Report the malaria status of this cell.
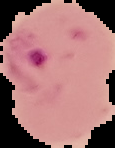
It is parasitized.

The area outside the segmented cell region is set to black. From a thin blood film. Image is 115×148 pixels.